Outline each Plasmodium ovale-infected red blood cell.
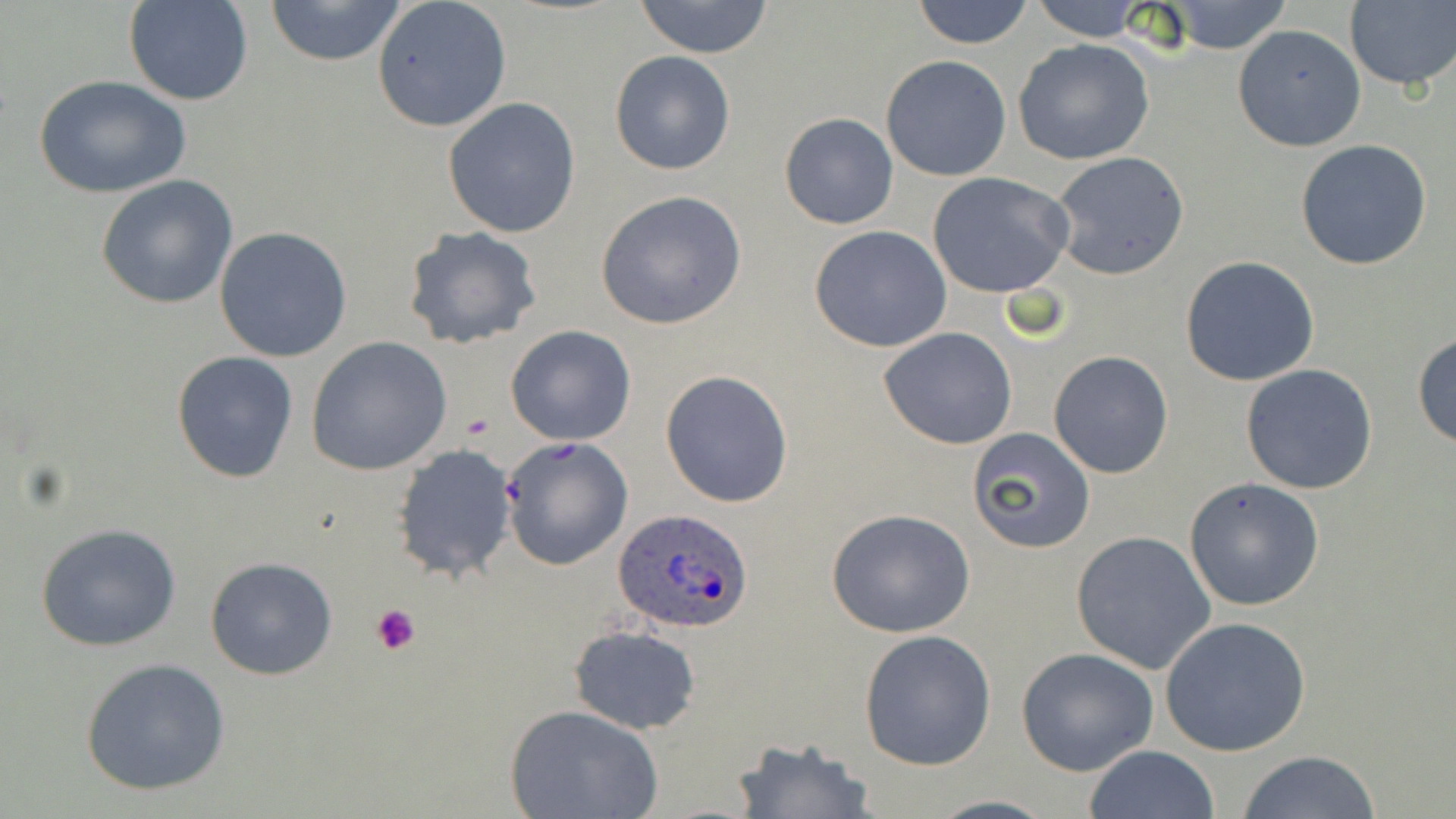
Approximate bounding boxes as named x1/y1/x2/y2 corners in pixels.
Plasmodium ovale-infected red blood cells: (x1=614, y1=508, x2=753, y2=634).

Summary:
  - Platelet locations: (x1=370, y1=602, x2=422, y2=656)
  - Uninfected red blood cell locations: (x1=125, y1=0, x2=254, y2=106), (x1=263, y1=0, x2=408, y2=68), (x1=632, y1=0, x2=775, y2=58), (x1=910, y1=0, x2=1036, y2=50), (x1=371, y1=1, x2=513, y2=132), (x1=1025, y1=1, x2=1160, y2=44), (x1=1156, y1=1, x2=1295, y2=54), (x1=1343, y1=2, x2=1456, y2=89), (x1=1233, y1=24, x2=1366, y2=152), (x1=1013, y1=39, x2=1156, y2=167), (x1=610, y1=51, x2=735, y2=176), (x1=881, y1=53, x2=1011, y2=180), (x1=33, y1=74, x2=192, y2=198), (x1=442, y1=97, x2=583, y2=238), (x1=779, y1=111, x2=899, y2=230), (x1=1295, y1=139, x2=1432, y2=270), (x1=1050, y1=150, x2=1189, y2=279), (x1=926, y1=172, x2=1075, y2=299), (x1=96, y1=175, x2=239, y2=309), (x1=594, y1=189, x2=747, y2=329), (x1=809, y1=225, x2=953, y2=353), (x1=213, y1=227, x2=353, y2=362), (x1=401, y1=227, x2=545, y2=351), (x1=1180, y1=256, x2=1320, y2=387), (x1=505, y1=326, x2=637, y2=446), (x1=879, y1=327, x2=1017, y2=449), (x1=1411, y1=332, x2=1456, y2=449), (x1=305, y1=336, x2=453, y2=476), (x1=171, y1=350, x2=300, y2=483), (x1=1048, y1=350, x2=1176, y2=479), (x1=1240, y1=364, x2=1379, y2=495), (x1=660, y1=369, x2=794, y2=507), (x1=967, y1=430, x2=1094, y2=552), (x1=500, y1=436, x2=634, y2=571), (x1=390, y1=444, x2=521, y2=584), (x1=1184, y1=477, x2=1326, y2=612), (x1=825, y1=508, x2=975, y2=638), (x1=36, y1=523, x2=185, y2=652), (x1=1070, y1=530, x2=1216, y2=675), (x1=206, y1=557, x2=338, y2=680), (x1=1159, y1=616, x2=1312, y2=756), (x1=568, y1=624, x2=703, y2=736), (x1=858, y1=629, x2=996, y2=771), (x1=1016, y1=646, x2=1160, y2=776), (x1=81, y1=658, x2=230, y2=797), (x1=505, y1=703, x2=663, y2=818), (x1=729, y1=736, x2=876, y2=819), (x1=1082, y1=746, x2=1219, y2=819), (x1=1235, y1=750, x2=1382, y2=819)
  - Slide-level diagnosis: Plasmodium ovale
  - Magnification: 1000x
  - Stain: May-Grünwald-Giemsa
  - Field of view: one of a larger specimen
  - Preparation: thin blood film
  - Modality: light microscopy
  - Image size: 1456×819 pixels